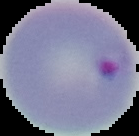
Summary:
  - Preparation: thin blood smear
  - Image size: 139×136 pixels
  - Malaria status: parasitized
  - Image type: cell region segmented out of the field of view; surrounding area masked to black